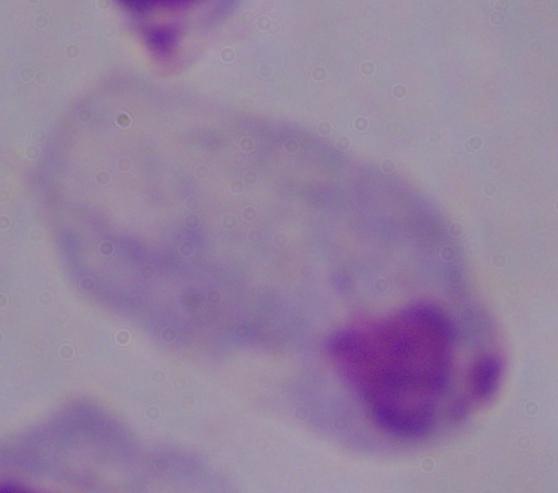

Summary:
  - Identification: trichomonad
  - Modality: photomicrograph
  - Magnification: 1000x